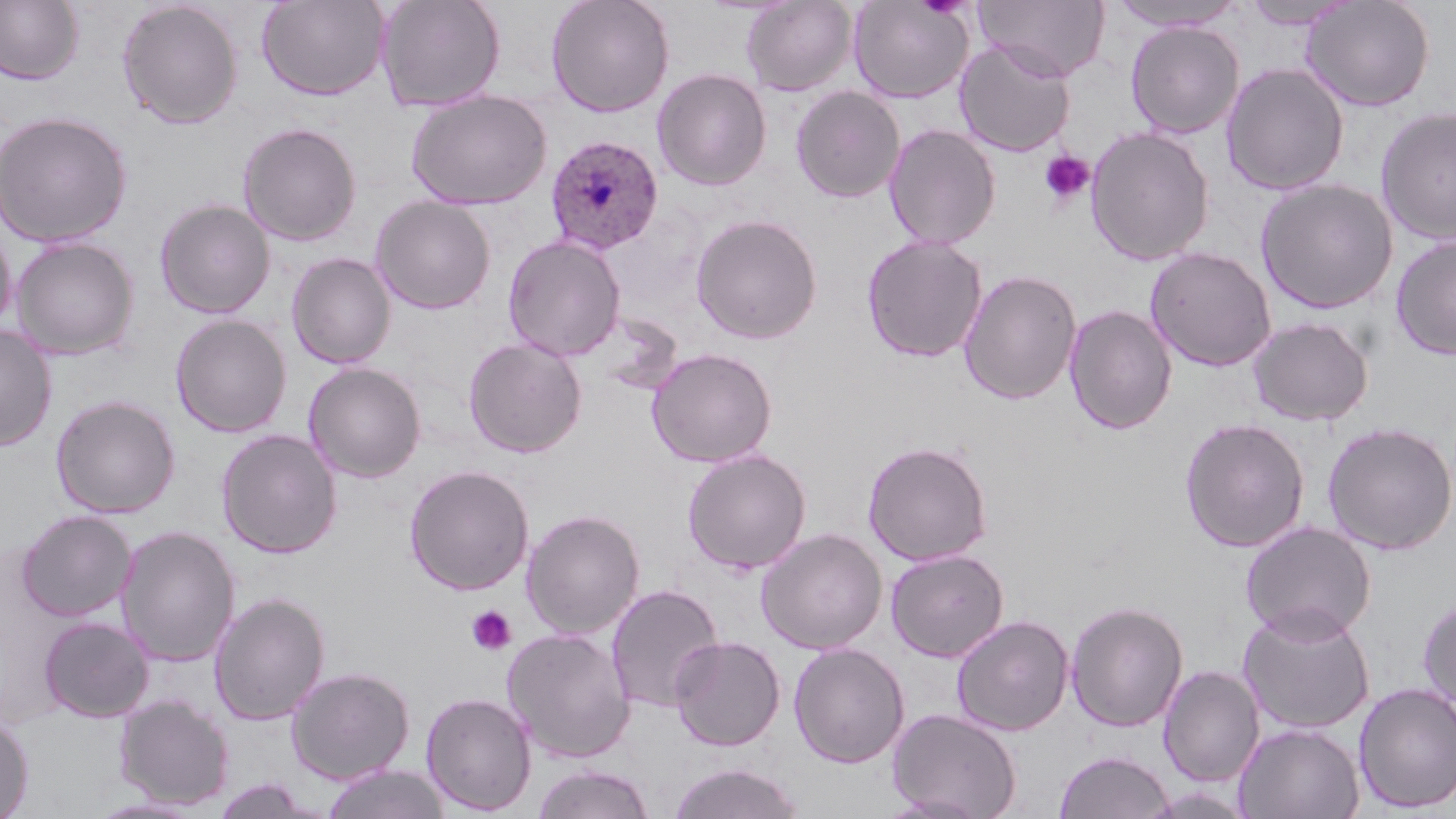

Approximate bounding boxes as named x1/y1/x2/y2 corners in pixels. Plasmodium ovale-infected red blood cell locations: (x1=545, y1=134, x2=664, y2=255). Uninfected red blood cell locations: (x1=0, y1=0, x2=84, y2=85), (x1=256, y1=0, x2=390, y2=101), (x1=376, y1=0, x2=506, y2=112), (x1=546, y1=0, x2=675, y2=118), (x1=740, y1=0, x2=858, y2=96), (x1=848, y1=0, x2=974, y2=104), (x1=977, y1=0, x2=1111, y2=82), (x1=1110, y1=0, x2=1247, y2=31), (x1=1300, y1=0, x2=1435, y2=112), (x1=117, y1=1, x2=243, y2=129), (x1=1242, y1=1, x2=1355, y2=30), (x1=1124, y1=20, x2=1245, y2=139), (x1=954, y1=39, x2=1076, y2=157), (x1=1221, y1=63, x2=1349, y2=195), (x1=652, y1=68, x2=773, y2=191), (x1=790, y1=85, x2=906, y2=203), (x1=406, y1=90, x2=552, y2=210), (x1=1375, y1=106, x2=1456, y2=247), (x1=0, y1=110, x2=134, y2=248), (x1=237, y1=122, x2=362, y2=246), (x1=883, y1=124, x2=1001, y2=249), (x1=1085, y1=126, x2=1214, y2=266), (x1=1255, y1=178, x2=1398, y2=314), (x1=370, y1=195, x2=496, y2=314), (x1=154, y1=198, x2=276, y2=319), (x1=691, y1=214, x2=823, y2=344), (x1=1, y1=219, x2=17, y2=337), (x1=861, y1=234, x2=987, y2=363), (x1=11, y1=235, x2=141, y2=360), (x1=502, y1=235, x2=627, y2=361), (x1=1390, y1=235, x2=1456, y2=360), (x1=1144, y1=246, x2=1277, y2=372), (x1=286, y1=252, x2=396, y2=369), (x1=959, y1=269, x2=1082, y2=405), (x1=1063, y1=305, x2=1178, y2=435), (x1=170, y1=314, x2=292, y2=438), (x1=1247, y1=316, x2=1374, y2=426), (x1=0, y1=324, x2=58, y2=451), (x1=463, y1=336, x2=587, y2=458), (x1=647, y1=347, x2=777, y2=468), (x1=303, y1=361, x2=427, y2=482), (x1=50, y1=394, x2=181, y2=519), (x1=1179, y1=417, x2=1311, y2=553), (x1=1321, y1=422, x2=1456, y2=555), (x1=216, y1=429, x2=342, y2=559), (x1=863, y1=440, x2=992, y2=566), (x1=682, y1=448, x2=812, y2=574), (x1=404, y1=464, x2=535, y2=595), (x1=522, y1=508, x2=645, y2=640), (x1=16, y1=510, x2=137, y2=621), (x1=1240, y1=521, x2=1376, y2=642), (x1=115, y1=525, x2=240, y2=667), (x1=756, y1=527, x2=887, y2=654), (x1=885, y1=548, x2=1009, y2=662), (x1=605, y1=583, x2=725, y2=714), (x1=209, y1=591, x2=331, y2=726), (x1=1418, y1=595, x2=1456, y2=714), (x1=1065, y1=600, x2=1189, y2=733), (x1=1237, y1=604, x2=1376, y2=734), (x1=951, y1=614, x2=1074, y2=736), (x1=38, y1=616, x2=154, y2=723), (x1=502, y1=627, x2=636, y2=763), (x1=669, y1=635, x2=786, y2=751), (x1=788, y1=642, x2=909, y2=768), (x1=1158, y1=665, x2=1265, y2=787), (x1=286, y1=666, x2=415, y2=785), (x1=1353, y1=682, x2=1456, y2=814), (x1=420, y1=691, x2=537, y2=815), (x1=114, y1=694, x2=234, y2=810), (x1=888, y1=707, x2=1022, y2=819), (x1=0, y1=713, x2=34, y2=819), (x1=1234, y1=722, x2=1364, y2=819), (x1=1054, y1=750, x2=1174, y2=819), (x1=667, y1=762, x2=806, y2=819), (x1=319, y1=763, x2=452, y2=819), (x1=531, y1=764, x2=657, y2=819), (x1=210, y1=777, x2=325, y2=819), (x1=86, y1=797, x2=209, y2=818). Platelet locations: (x1=1039, y1=150, x2=1095, y2=207), (x1=466, y1=605, x2=517, y2=656). Slide-level diagnosis: Plasmodium ovale. May-Grünwald-Giemsa-stained preparation. Captured at 1000x magnification. Image is 1456×819 pixels. Light microscopy. Thin blood film. Single field of view.